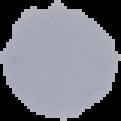
Result: no malaria parasites seen. From a thin blood film. Segmented cell region on a black background. Image is 121×121 pixels.